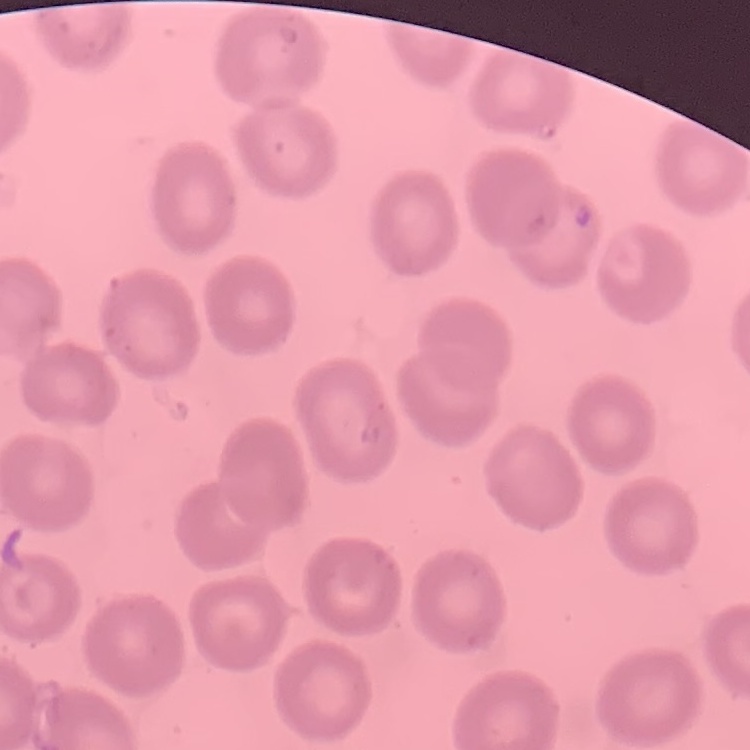

The erythrocytes exhibit no rouleaux formation. One tile cut from a larger photomicrograph. Thin blood smear. Field's or Giemsa stain.